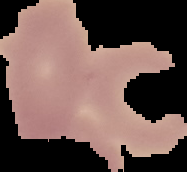

{
  "preparation": "thin blood smear",
  "image_size": "187×172 pixels",
  "malaria_status": "uninfected",
  "image_type": "segmented cell region on a black background"
}